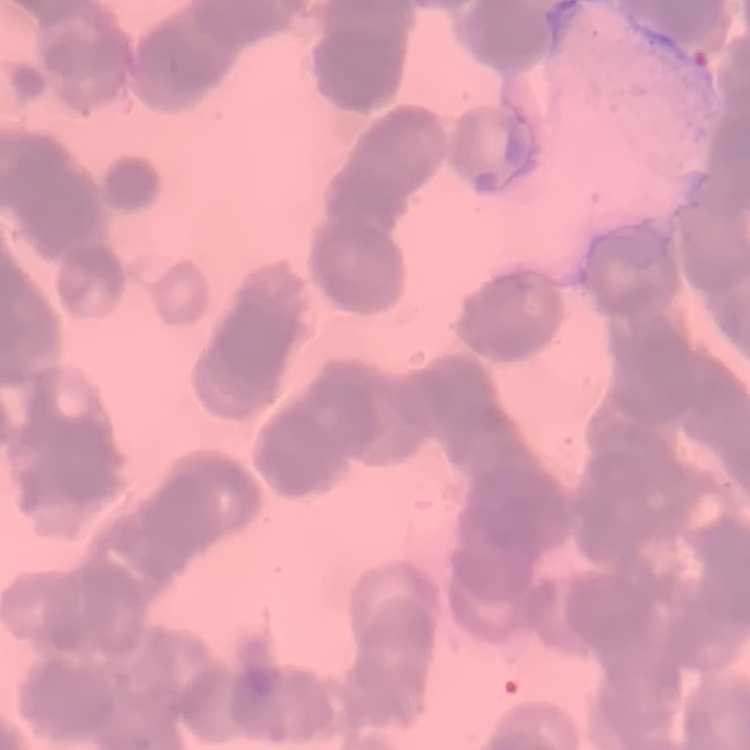
Summary:
  - Red blood cell morphology: rouleaux formation
  - Image type: square crop of a larger photomicrograph
  - Stain: Field's or Giemsa
  - Preparation: thin peripheral smear